Give the extent of all Plasmodium vivax-infected red blood cells.
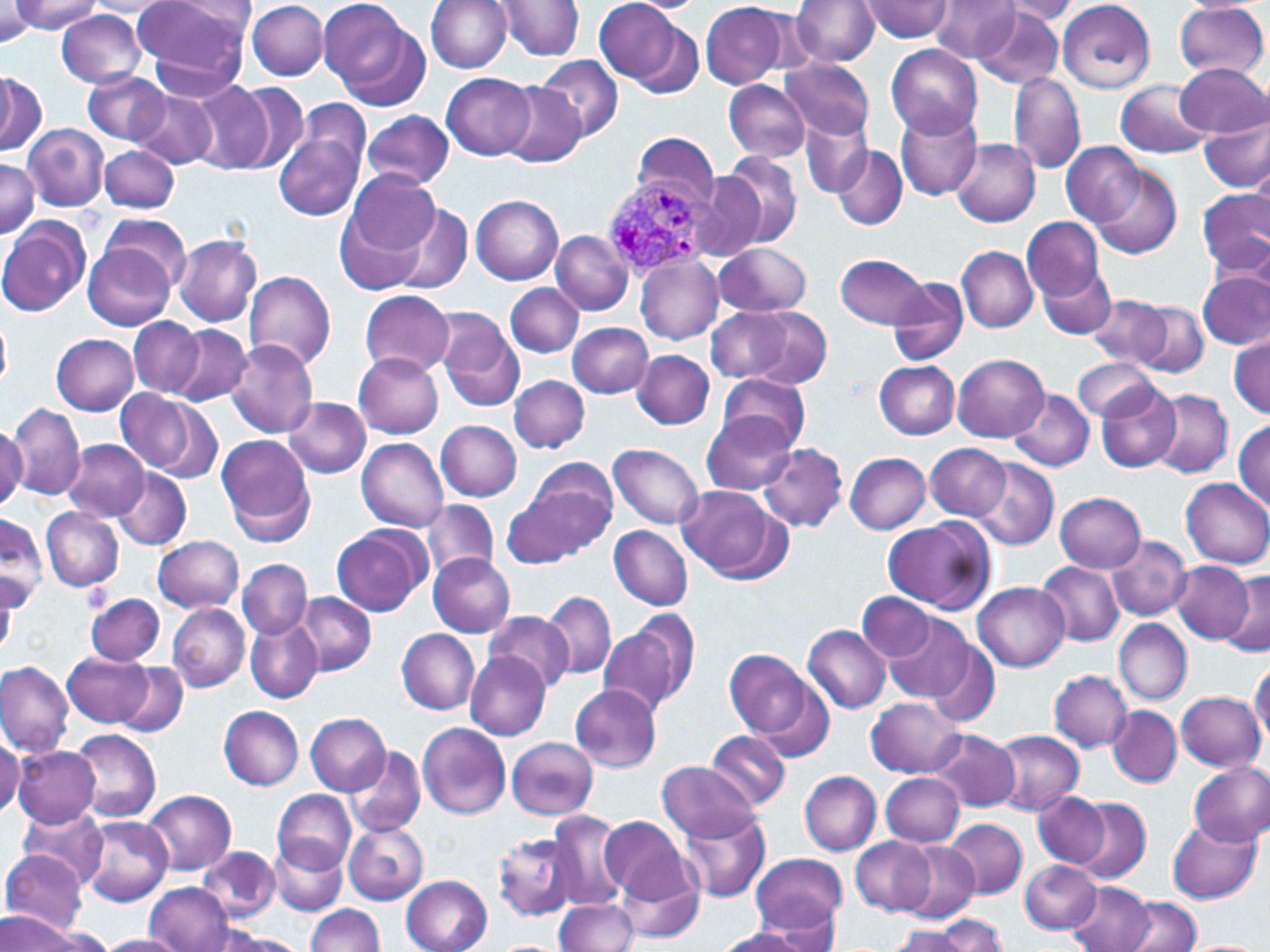

Approximate bounding boxes as named x1/y1/x2/y2 corners in pixels.
Plasmodium vivax-infected red blood cells: (x1=600, y1=172, x2=717, y2=279).

slide-level diagnosis = Plasmodium vivax
uninfected red blood cell locations = approximate bounding boxes as named x1/y1/x2/y2 corners in pixels: (x1=10, y1=0, x2=102, y2=33), (x1=132, y1=0, x2=253, y2=87), (x1=317, y1=0, x2=423, y2=102), (x1=425, y1=0, x2=513, y2=72), (x1=495, y1=0, x2=585, y2=60), (x1=594, y1=0, x2=687, y2=86), (x1=625, y1=0, x2=703, y2=14), (x1=791, y1=0, x2=877, y2=67), (x1=856, y1=0, x2=957, y2=41), (x1=930, y1=0, x2=1019, y2=63), (x1=1057, y1=0, x2=1156, y2=93), (x1=83, y1=1, x2=172, y2=16), (x1=247, y1=1, x2=327, y2=80), (x1=1, y1=2, x2=37, y2=43), (x1=700, y1=2, x2=791, y2=88), (x1=998, y1=2, x2=1080, y2=24), (x1=1174, y1=2, x2=1268, y2=79), (x1=972, y1=8, x2=1065, y2=89), (x1=55, y1=10, x2=148, y2=87), (x1=627, y1=17, x2=706, y2=96), (x1=885, y1=43, x2=983, y2=139), (x1=536, y1=57, x2=623, y2=143), (x1=780, y1=58, x2=875, y2=140), (x1=1176, y1=62, x2=1267, y2=137), (x1=81, y1=69, x2=171, y2=144), (x1=1008, y1=69, x2=1086, y2=175), (x1=0, y1=71, x2=47, y2=155), (x1=442, y1=73, x2=535, y2=160), (x1=724, y1=79, x2=811, y2=163), (x1=1115, y1=80, x2=1212, y2=158), (x1=189, y1=81, x2=273, y2=173), (x1=499, y1=82, x2=583, y2=167), (x1=232, y1=84, x2=310, y2=173), (x1=129, y1=89, x2=218, y2=170), (x1=296, y1=98, x2=370, y2=175), (x1=895, y1=108, x2=983, y2=200), (x1=363, y1=110, x2=453, y2=191), (x1=800, y1=111, x2=873, y2=198), (x1=1200, y1=113, x2=1270, y2=192), (x1=24, y1=124, x2=109, y2=211), (x1=274, y1=130, x2=365, y2=222), (x1=629, y1=131, x2=719, y2=211), (x1=951, y1=140, x2=1039, y2=226), (x1=1062, y1=141, x2=1144, y2=226), (x1=831, y1=145, x2=907, y2=231), (x1=99, y1=146, x2=180, y2=213), (x1=718, y1=150, x2=803, y2=249), (x1=0, y1=157, x2=39, y2=239), (x1=1091, y1=167, x2=1182, y2=259), (x1=345, y1=170, x2=439, y2=256), (x1=684, y1=172, x2=765, y2=263), (x1=1199, y1=188, x2=1270, y2=276), (x1=471, y1=195, x2=564, y2=284), (x1=389, y1=203, x2=471, y2=293), (x1=334, y1=207, x2=426, y2=295), (x1=102, y1=215, x2=190, y2=290), (x1=1022, y1=217, x2=1103, y2=300), (x1=0, y1=219, x2=88, y2=316), (x1=551, y1=230, x2=632, y2=315), (x1=173, y1=235, x2=261, y2=326), (x1=714, y1=243, x2=811, y2=317), (x1=84, y1=244, x2=173, y2=329), (x1=957, y1=246, x2=1037, y2=332), (x1=836, y1=253, x2=932, y2=328), (x1=635, y1=256, x2=723, y2=345), (x1=1037, y1=262, x2=1115, y2=339), (x1=243, y1=269, x2=337, y2=371), (x1=1199, y1=273, x2=1269, y2=349), (x1=887, y1=276, x2=968, y2=366), (x1=505, y1=282, x2=584, y2=357), (x1=360, y1=290, x2=453, y2=375), (x1=1088, y1=294, x2=1174, y2=369), (x1=1134, y1=302, x2=1209, y2=376), (x1=706, y1=307, x2=795, y2=382), (x1=743, y1=307, x2=833, y2=388), (x1=434, y1=309, x2=526, y2=412), (x1=127, y1=315, x2=204, y2=396), (x1=0, y1=319, x2=12, y2=393), (x1=567, y1=321, x2=653, y2=398), (x1=170, y1=324, x2=251, y2=405), (x1=51, y1=332, x2=138, y2=416), (x1=1230, y1=333, x2=1268, y2=418), (x1=224, y1=340, x2=318, y2=437), (x1=632, y1=349, x2=714, y2=429), (x1=354, y1=354, x2=444, y2=438), (x1=953, y1=354, x2=1047, y2=441), (x1=1072, y1=359, x2=1161, y2=420), (x1=875, y1=360, x2=959, y2=438), (x1=718, y1=373, x2=812, y2=453), (x1=509, y1=374, x2=589, y2=452), (x1=1095, y1=379, x2=1182, y2=472), (x1=1009, y1=389, x2=1095, y2=470), (x1=1150, y1=389, x2=1233, y2=478), (x1=116, y1=390, x2=192, y2=471), (x1=284, y1=396, x2=371, y2=478), (x1=147, y1=399, x2=222, y2=482), (x1=4, y1=402, x2=85, y2=498), (x1=701, y1=411, x2=797, y2=495), (x1=437, y1=420, x2=522, y2=501), (x1=1235, y1=420, x2=1269, y2=513), (x1=0, y1=425, x2=26, y2=507), (x1=217, y1=435, x2=314, y2=537), (x1=358, y1=438, x2=449, y2=530), (x1=929, y1=438, x2=1035, y2=577), (x1=64, y1=440, x2=148, y2=521), (x1=924, y1=442, x2=1011, y2=520), (x1=610, y1=443, x2=705, y2=528), (x1=758, y1=443, x2=850, y2=531), (x1=846, y1=453, x2=930, y2=533), (x1=521, y1=457, x2=620, y2=556), (x1=971, y1=458, x2=1058, y2=549), (x1=113, y1=467, x2=191, y2=549), (x1=1181, y1=477, x2=1270, y2=566), (x1=677, y1=485, x2=785, y2=581), (x1=502, y1=491, x2=587, y2=568), (x1=1055, y1=492, x2=1146, y2=572), (x1=422, y1=500, x2=498, y2=583), (x1=42, y1=508, x2=124, y2=592), (x1=0, y1=512, x2=45, y2=606), (x1=882, y1=517, x2=991, y2=612), (x1=332, y1=526, x2=424, y2=617), (x1=609, y1=526, x2=693, y2=609), (x1=153, y1=535, x2=243, y2=612), (x1=1106, y1=537, x2=1192, y2=619), (x1=1037, y1=551, x2=1187, y2=630), (x1=428, y1=555, x2=514, y2=636), (x1=238, y1=559, x2=312, y2=639), (x1=1170, y1=560, x2=1255, y2=643), (x1=1038, y1=561, x2=1123, y2=646), (x1=1225, y1=569, x2=1270, y2=654), (x1=974, y1=582, x2=1068, y2=671), (x1=541, y1=591, x2=617, y2=679), (x1=85, y1=592, x2=165, y2=665), (x1=297, y1=593, x2=375, y2=675), (x1=859, y1=593, x2=936, y2=664), (x1=169, y1=602, x2=250, y2=691), (x1=624, y1=606, x2=702, y2=703), (x1=485, y1=613, x2=574, y2=693), (x1=881, y1=613, x2=977, y2=703), (x1=245, y1=616, x2=322, y2=702), (x1=1114, y1=619, x2=1190, y2=704), (x1=598, y1=623, x2=685, y2=718), (x1=803, y1=624, x2=891, y2=715), (x1=397, y1=628, x2=481, y2=714), (x1=922, y1=636, x2=1001, y2=729), (x1=465, y1=650, x2=550, y2=740), (x1=724, y1=650, x2=814, y2=739), (x1=61, y1=651, x2=153, y2=727), (x1=1249, y1=659, x2=1269, y2=746), (x1=0, y1=661, x2=74, y2=757), (x1=116, y1=663, x2=189, y2=735), (x1=1049, y1=670, x2=1131, y2=751), (x1=749, y1=678, x2=837, y2=764), (x1=569, y1=685, x2=661, y2=771), (x1=1175, y1=691, x2=1264, y2=770), (x1=867, y1=696, x2=965, y2=778), (x1=218, y1=705, x2=305, y2=790), (x1=1108, y1=706, x2=1181, y2=786), (x1=304, y1=713, x2=389, y2=795), (x1=419, y1=723, x2=510, y2=819), (x1=928, y1=728, x2=1020, y2=812), (x1=71, y1=729, x2=161, y2=821), (x1=991, y1=729, x2=1085, y2=814), (x1=705, y1=730, x2=790, y2=810), (x1=0, y1=734, x2=23, y2=819), (x1=506, y1=737, x2=598, y2=819), (x1=1017, y1=742, x2=1099, y2=872), (x1=345, y1=744, x2=426, y2=835), (x1=13, y1=745, x2=99, y2=829), (x1=656, y1=760, x2=760, y2=841), (x1=1189, y1=762, x2=1270, y2=847), (x1=799, y1=770, x2=881, y2=856), (x1=881, y1=772, x2=963, y2=846), (x1=141, y1=788, x2=236, y2=875), (x1=272, y1=789, x2=355, y2=871), (x1=1034, y1=793, x2=1109, y2=867), (x1=1073, y1=797, x2=1151, y2=883), (x1=18, y1=806, x2=107, y2=886), (x1=545, y1=811, x2=627, y2=911), (x1=681, y1=811, x2=771, y2=901), (x1=78, y1=814, x2=173, y2=907), (x1=600, y1=815, x2=691, y2=901), (x1=1167, y1=816, x2=1261, y2=905), (x1=944, y1=817, x2=1027, y2=900), (x1=342, y1=822, x2=429, y2=904), (x1=495, y1=832, x2=577, y2=921), (x1=269, y1=836, x2=349, y2=915), (x1=851, y1=837, x2=936, y2=915), (x1=901, y1=841, x2=979, y2=923), (x1=198, y1=846, x2=279, y2=920), (x1=1, y1=848, x2=89, y2=935), (x1=751, y1=853, x2=846, y2=935), (x1=615, y1=859, x2=704, y2=942), (x1=1019, y1=859, x2=1101, y2=933), (x1=403, y1=876, x2=492, y2=952), (x1=144, y1=882, x2=234, y2=952), (x1=1066, y1=882, x2=1153, y2=952), (x1=554, y1=896, x2=639, y2=951), (x1=1124, y1=896, x2=1201, y2=952), (x1=304, y1=904, x2=385, y2=952), (x1=2, y1=912, x2=84, y2=952), (x1=936, y1=913, x2=1006, y2=951), (x1=26, y1=925, x2=112, y2=951), (x1=887, y1=926, x2=970, y2=951), (x1=713, y1=928, x2=811, y2=952), (x1=214, y1=931, x2=309, y2=952), (x1=99, y1=935, x2=185, y2=952)
stain = May-Grünwald-Giemsa
field of view = one of a larger specimen
magnification = 1000x
image size = 1270×952 pixels
preparation = thin blood film
modality = optical microscopy